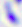
magnification = 400x
modality = micrograph
identification = Toxoplasma gondii